Identify the parasite.
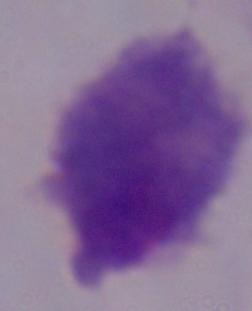

A trichomonad.

magnification = 1000x
modality = micrograph